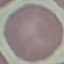

Summary:
  - Result: no malaria parasites detected
  - Capture: smartphone camera at the microscope eyepiece
  - Preparation: thin blood smear
  - Stain: Giemsa
  - Image type: automatically extracted cell patch, resized to 64 × 64 pixels